Classify this cell by malaria status.
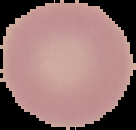
It is uninfected.

{
  "image_size": "136×130 pixels",
  "image_type": "segmented cell region on a black background",
  "preparation": "thin blood smear"
}